Give the extent of all Plasmodium falciparum-infected red blood cells.
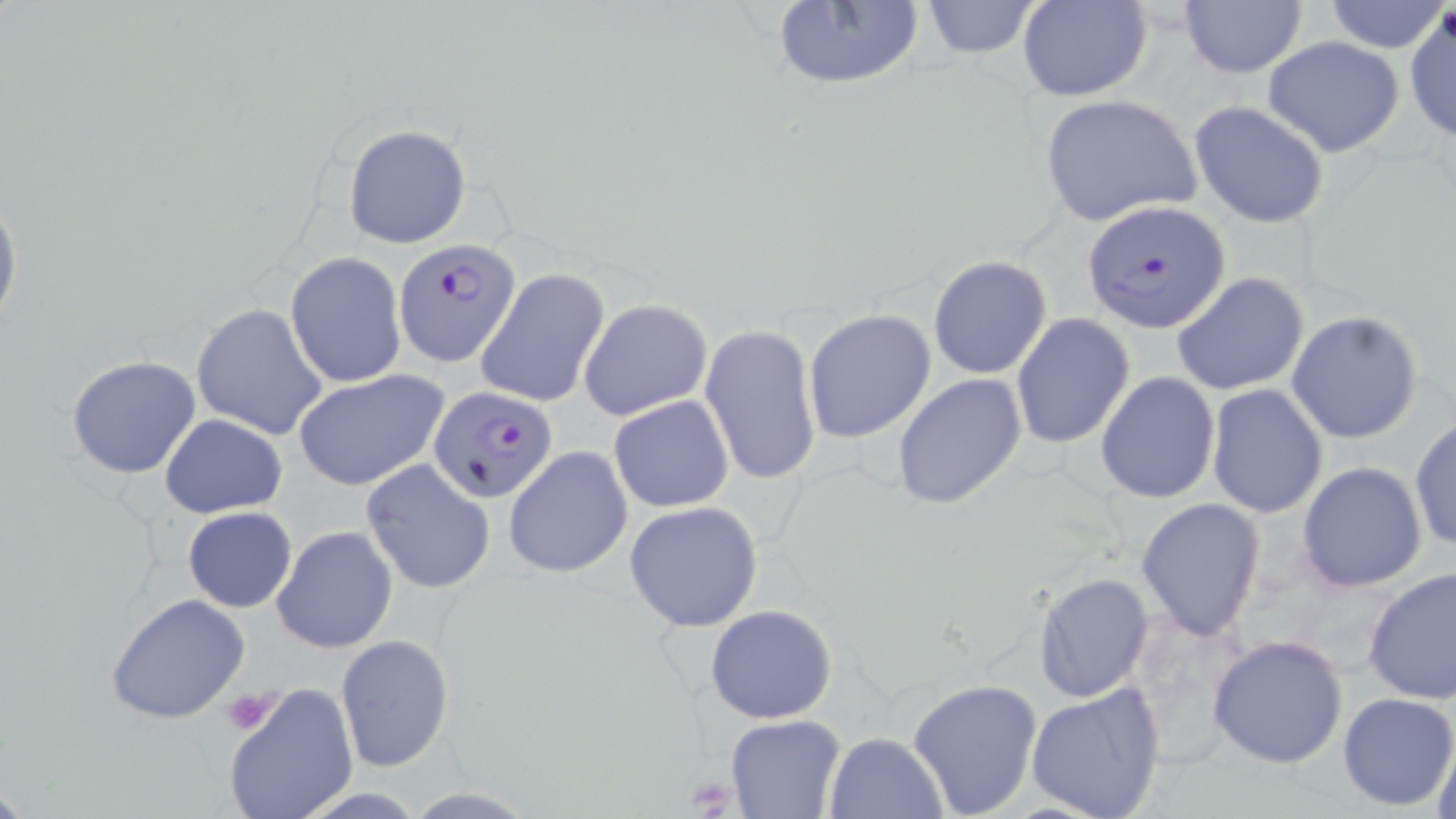

Approximate bounding boxes as (x1,y1)-(x2,y2) corner pairs in pixels.
Plasmodium falciparum-infected red blood cells: (1081,198)-(1233,334), (393,241)-(523,366), (430,384)-(558,503).

Summary:
  - Uninfected red blood cell locations: (768,0)-(925,92), (919,0)-(1045,58), (1017,0)-(1153,102), (1178,0)-(1309,79), (1322,1)-(1448,53), (1404,6)-(1456,144), (1263,35)-(1405,158), (1039,93)-(1203,229), (1188,100)-(1330,231), (343,124)-(471,249), (0,182)-(22,342), (286,253)-(407,388), (928,255)-(1052,378), (475,267)-(610,407), (1171,271)-(1309,397), (579,298)-(714,420), (191,303)-(328,441), (803,309)-(937,444), (1284,310)-(1425,445), (1010,313)-(1136,450), (700,323)-(820,487), (66,356)-(200,479), (294,368)-(449,491), (1096,371)-(1220,505), (892,373)-(1026,510), (1206,384)-(1329,519), (609,394)-(733,511), (159,414)-(288,518), (1409,414)-(1456,553), (504,445)-(634,579), (360,458)-(497,594), (1297,461)-(1428,593), (1136,497)-(1266,642), (624,501)-(766,633), (182,506)-(297,611), (271,525)-(398,653), (1362,567)-(1456,706), (1031,571)-(1153,703), (105,592)-(251,725), (705,604)-(838,724), (1205,632)-(1350,769), (335,634)-(454,773), (908,678)-(1042,818), (221,682)-(360,819), (1025,684)-(1168,819), (1336,692)-(1456,809), (724,714)-(847,819), (1431,725)-(1456,819), (823,732)-(948,819)
  - Platelet locations: (221,688)-(284,735), (685,775)-(739,815)
  - Slide-level diagnosis: Plasmodium falciparum
  - Stain: May-Grünwald-Giemsa
  - Modality: light microscopy
  - Image size: 1456×819 pixels
  - Preparation: thin blood smear
  - Field of view: single
  - Magnification: 1000x